State which parasite is depicted.
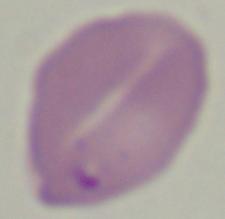

This is Babesia.

modality = micrograph
magnification = 1000x